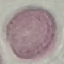

Summary:
  - Result: no malaria parasites seen
  - Capture: smartphone through the microscope eyepiece
  - Image type: automatically extracted cell patch, resized to 64 × 64 pixels
  - Preparation: thin smear
  - Stain: Giemsa